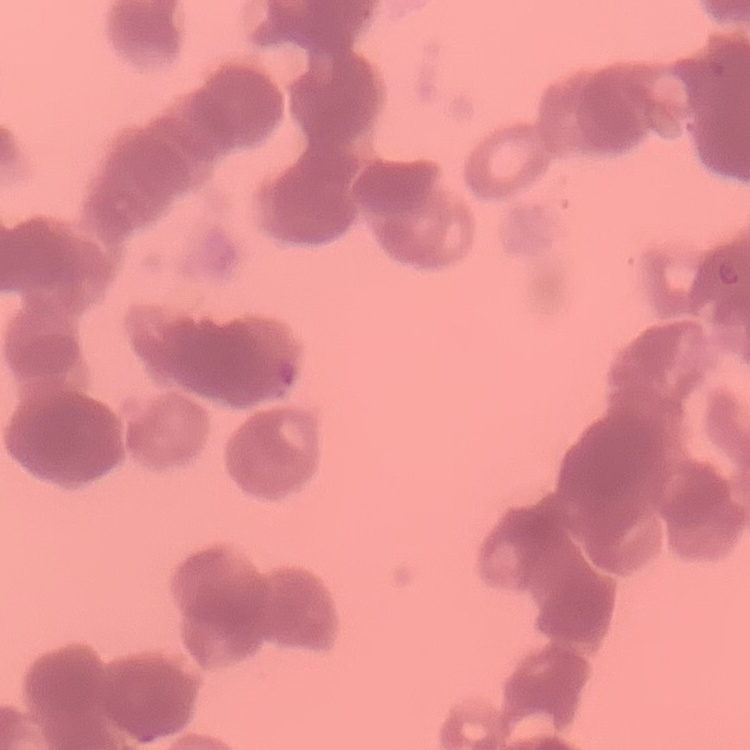
The red blood cells exhibit rouleaux formation. Stained with either Field's or Giemsa. Thin blood film. Square crop of a larger photomicrograph.